Comment on the morphology of the erythrocytes.
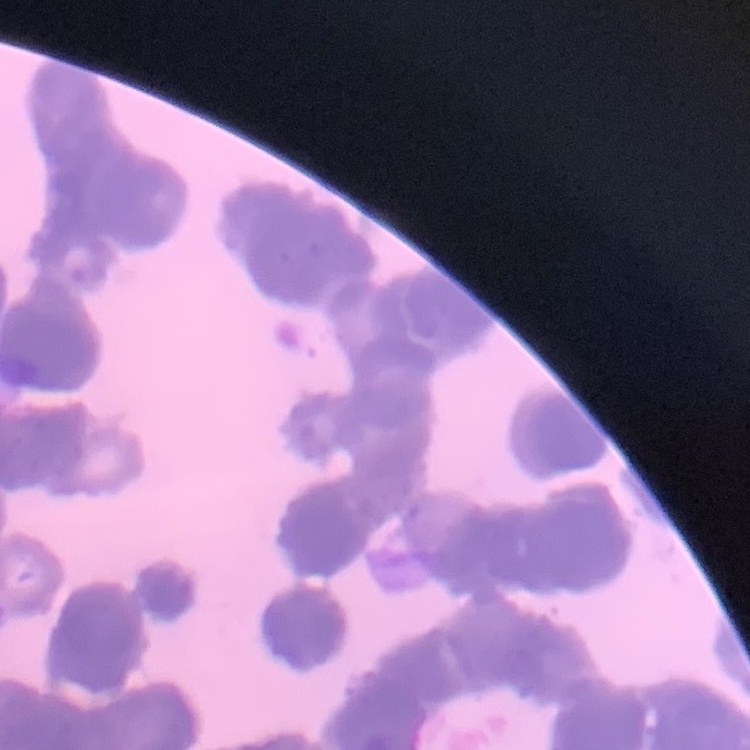

They show rouleaux formation.

Thin blood smear. One tile cut from a larger photomicrograph. Stained with either Field's or Giemsa.